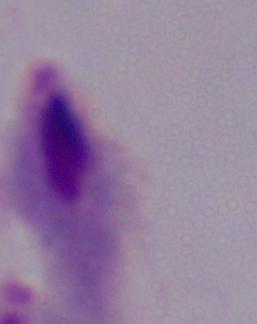
Captured at 1000x magnification. Micrograph. A trichomonad is shown.